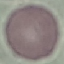
Malaria status: uninfected. Photographed with a smartphone camera at the microscope eyepiece. Giemsa-stained preparation. Thin smear of blood. Cell patch, automatically extracted from a larger field of view and resized to 64 × 64 pixels.